Report the malaria status of this cell.
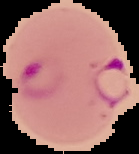
It is parasitized.

Summary:
  - Image size: 139×154 pixels
  - Preparation: thin blood film
  - Image type: segmented cell region with the area outside set to black